Assess this cell for malaria.
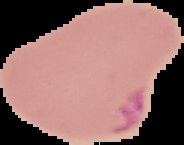

Parasitized.

Summary:
  - Image type: segmented cell region with the area outside set to black
  - Image size: 184×145 pixels
  - Preparation: thin blood smear